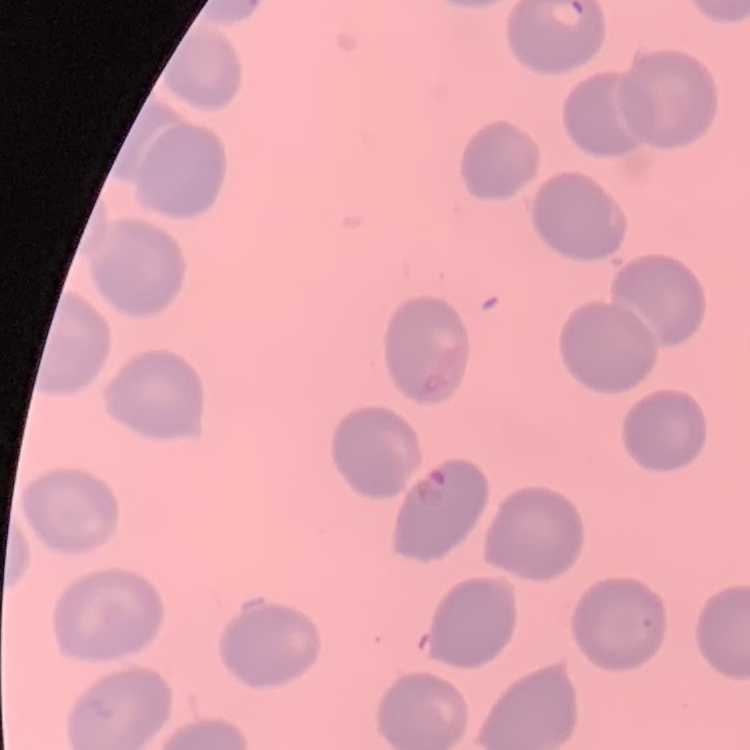
Summary:
  - Red blood cell morphology: no rouleaux formation
  - Preparation: thin peripheral smear
  - Image type: square crop of a larger photomicrograph
  - Stain: Field's or Giemsa